Locate every malaria parasite.
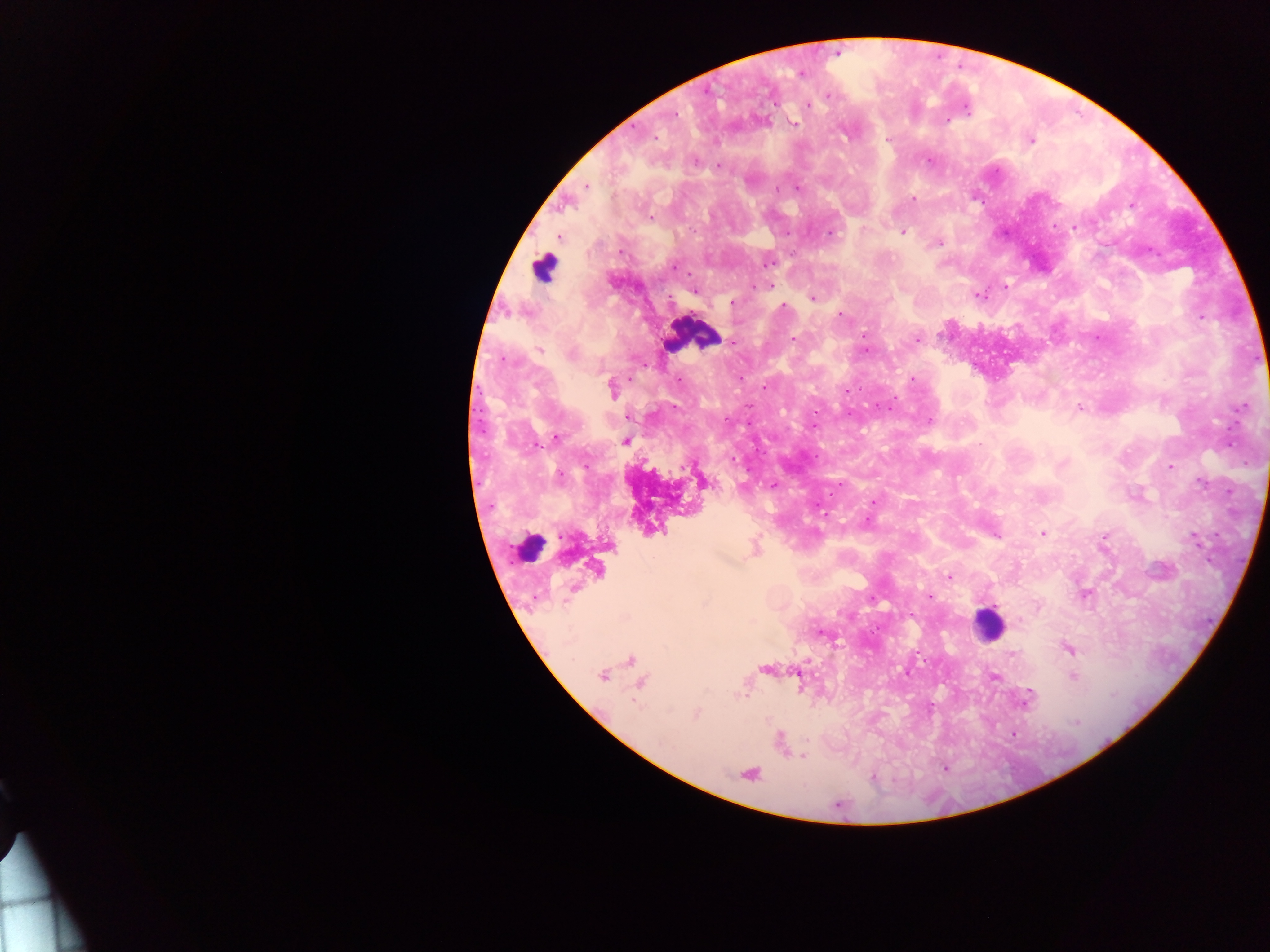

Approximate centers as x y in pixels.
Malaria parasites: 827 99; 808 104; 964 106; 677 115; 763 120; 794 123; 944 123; 632 128; 847 132; 886 138; 655 139; 1032 139; 694 160; 928 161; 718 166; 797 186; 587 187; 913 198; 981 201; 650 218; 1075 223; 1056 226; 829 232; 902 232; 789 234; 941 242; 620 249; 1149 252; 768 261; 676 265; 757 285; 766 285; 1005 287; 694 291; 979 295; 812 298; 732 303; 784 307; 839 316; 1201 317; 1096 337; 794 338; 917 338; 865 346; 573 354; 678 378; 914 379; 766 384; 860 389; 891 404; 1078 406; 673 408; 1241 408; 849 413; 628 416; 726 418; 929 420; 813 426; 557 437; 1228 447; 756 450; 734 459; 1245 463; 1063 464; 1171 466; 773 485; 1201 485; 1230 490; 830 495; 872 500; 1041 534; 997 536; 1105 536; 1217 536; 949 575; 1083 595; 929 596; 1039 606; 625 616; 819 632; 838 642; 1071 649; 1075 653; 923 659; 904 673; 997 677; 1073 678; 705 692; 746 692; 1030 692; 740 694; 632 704; 934 705; 670 711; 695 716; 768 719; 1075 720; 1010 735; 804 754; 802 757; 944 768.

capture = mobile-phone photograph through a microscope
country = Ghana
leukocyte locations = approximate centers as x y in pixels: 548 267; 692 333; 526 552; 988 627
preparation = thick blood smear
image size = 1270×952 pixels
field of view = single